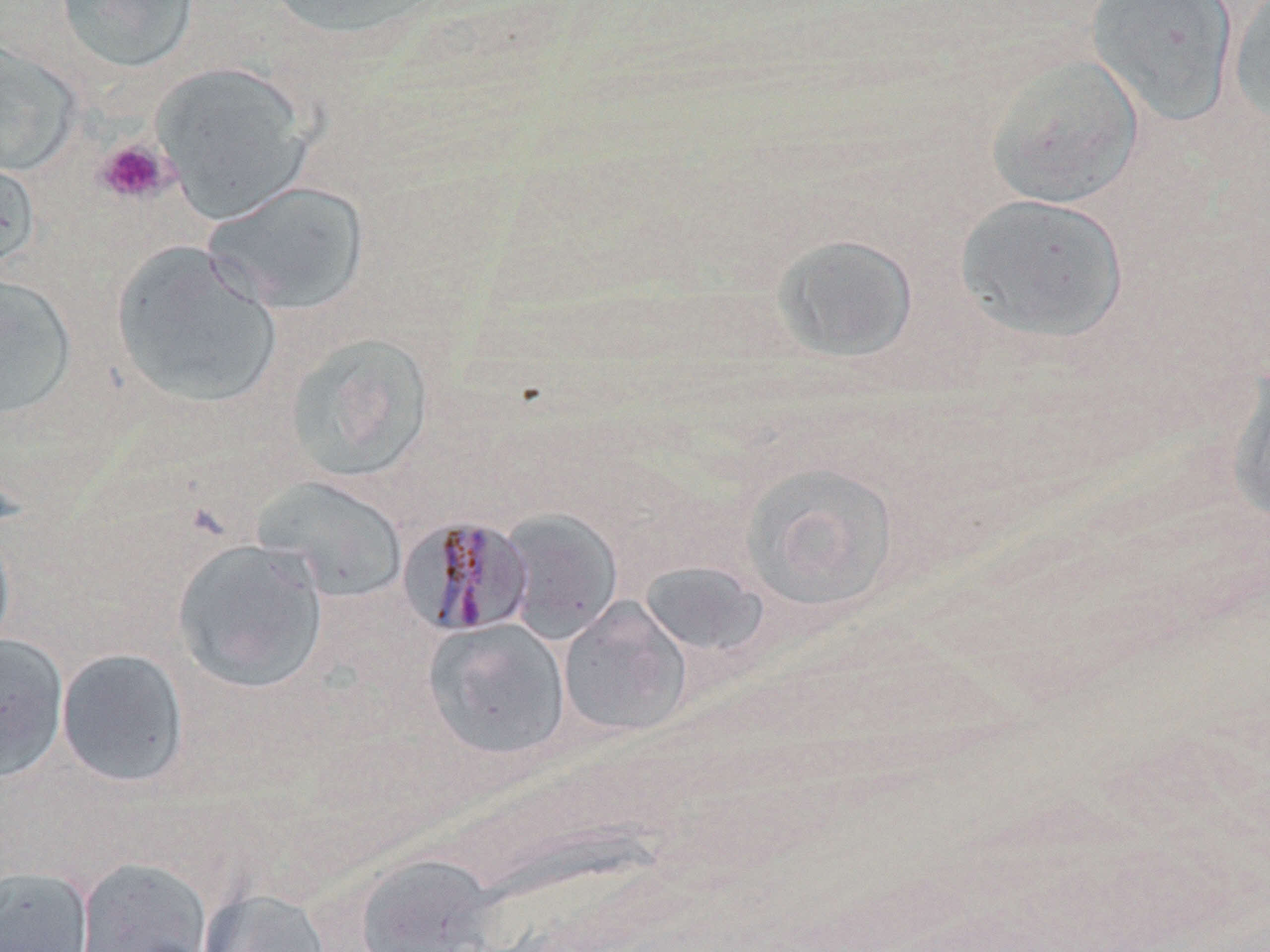

{
  "slide_level_diagnosis": "Plasmodium malariae",
  "modality": "optical microscopy",
  "uninfected_red_blood_cell_locations": "approximate bounding boxes as (x1, y1, x2, y2) in pixels: (55, 0, 199, 74), (263, 0, 442, 43), (1084, 0, 1238, 126), (1227, 0, 1270, 128), (0, 40, 82, 177), (984, 52, 1145, 209), (149, 61, 316, 223), (0, 151, 40, 276), (203, 181, 370, 315), (955, 192, 1130, 343), (772, 234, 919, 362), (110, 241, 282, 409), (0, 274, 77, 420), (284, 333, 436, 484), (1225, 368, 1270, 525), (740, 462, 900, 614), (254, 477, 408, 603), (499, 508, 623, 644), (0, 517, 16, 662), (172, 539, 328, 693), (638, 561, 769, 661), (558, 599, 692, 738), (423, 619, 571, 760), (0, 633, 69, 781), (56, 648, 190, 789), (353, 853, 501, 952), (74, 856, 213, 951), (0, 864, 94, 952), (197, 887, 331, 952)",
  "magnification": "1000x",
  "platelet_locations": "approximate bounding boxes as (x1, y1, x2, y2) in pixels: (94, 138, 174, 205)",
  "field_of_view": "single",
  "preparation": "thin blood film",
  "image_size": "1270×952 pixels",
  "stain": "May-Grünwald-Giemsa",
  "plasmodium_malariae_infected_red_blood_cell_locations": "approximate bounding boxes as (x1, y1, x2, y2) in pixels: (398, 515, 534, 637)"
}